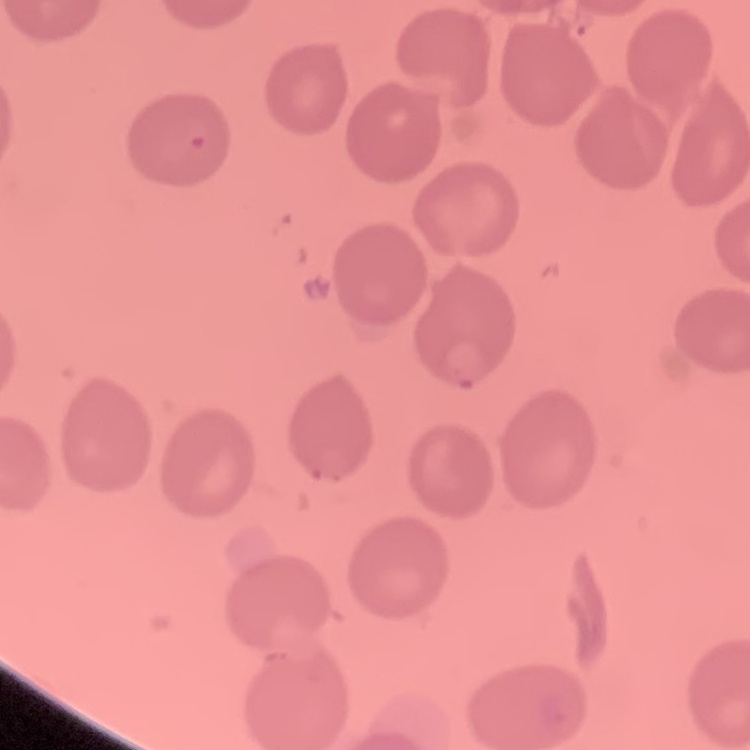
Summary:
  - Erythrocyte morphology: no rouleaux formation
  - Preparation: thin peripheral smear
  - Image type: square crop of a larger photomicrograph
  - Stain: Field's or Giemsa